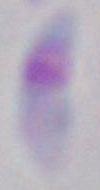 Toxoplasma gondii is seen. Photomicrograph. 1000x magnification.